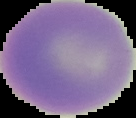

Summary:
  - Image type: cell region segmented out of the field of view; surrounding area masked to black
  - Preparation: thin blood smear
  - Malaria status: uninfected
  - Image size: 136×118 pixels